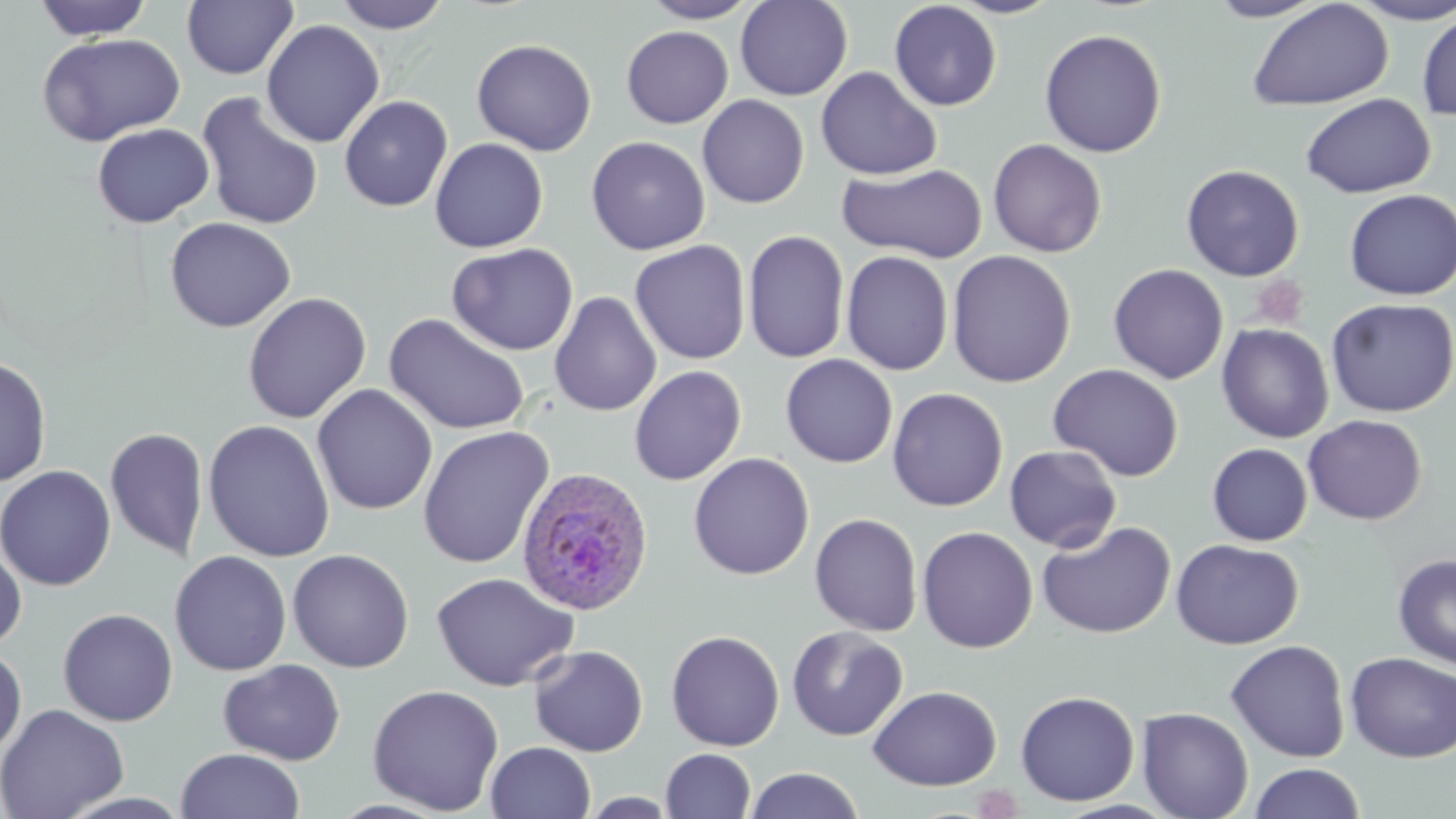
Approximate bounding boxes as [x1, y1, x2, y2] in pixels. Platelet locations: [1249, 275, 1309, 330]. Plasmodium ovale-infected red blood cell locations: [516, 466, 655, 617]. Uninfected red blood cell locations: [33, 0, 153, 40], [182, 0, 298, 80], [332, 0, 453, 33], [640, 0, 761, 23], [735, 0, 853, 101], [946, 0, 1064, 19], [1206, 0, 1328, 22], [1346, 0, 1456, 24], [889, 1, 1001, 111], [1246, 1, 1394, 112], [1416, 9, 1456, 121], [261, 19, 385, 148], [622, 25, 733, 128], [1039, 28, 1167, 158], [36, 32, 187, 146], [471, 38, 597, 156], [815, 66, 941, 180], [196, 92, 325, 231], [1301, 93, 1435, 198], [340, 95, 452, 212], [697, 95, 809, 209], [91, 123, 215, 228], [586, 136, 711, 255], [430, 138, 549, 253], [987, 138, 1107, 257], [836, 163, 988, 263], [1179, 164, 1303, 281], [1343, 189, 1456, 300], [164, 217, 296, 332], [743, 230, 850, 364], [629, 240, 751, 365], [447, 243, 578, 356], [841, 250, 954, 376], [947, 250, 1076, 388], [1108, 263, 1229, 385], [549, 291, 661, 416], [242, 292, 372, 423], [1326, 297, 1456, 418], [383, 313, 531, 436], [1216, 323, 1334, 443], [780, 354, 898, 468], [0, 355, 52, 488], [1047, 363, 1183, 482], [627, 365, 747, 486], [312, 383, 438, 516], [887, 387, 1008, 511], [1303, 415, 1427, 525], [202, 419, 336, 562], [417, 426, 555, 569], [104, 427, 208, 561], [1207, 443, 1313, 546], [1004, 444, 1122, 553], [688, 453, 814, 580], [0, 465, 117, 591], [809, 513, 923, 636], [1036, 520, 1176, 639], [917, 526, 1038, 653], [1171, 539, 1303, 649], [0, 544, 27, 651], [287, 549, 414, 673], [170, 550, 292, 677], [1392, 554, 1456, 671], [431, 571, 579, 692], [57, 608, 178, 726], [787, 625, 908, 741], [666, 630, 785, 752], [1226, 639, 1350, 762], [0, 644, 27, 760], [529, 645, 648, 756], [1345, 652, 1456, 762], [218, 659, 345, 765], [367, 684, 505, 815], [867, 685, 1002, 791], [1015, 690, 1140, 806], [1, 704, 129, 819], [1137, 706, 1253, 819], [486, 741, 596, 819], [175, 747, 305, 819], [660, 749, 756, 818], [1248, 763, 1366, 819], [744, 767, 865, 819]. Slide-level diagnosis: Plasmodium ovale. Image is 1456×819 pixels. May-Grünwald-Giemsa stain. Single field of view. Light microscopy. Captured at 1000x magnification. Thin blood smear.